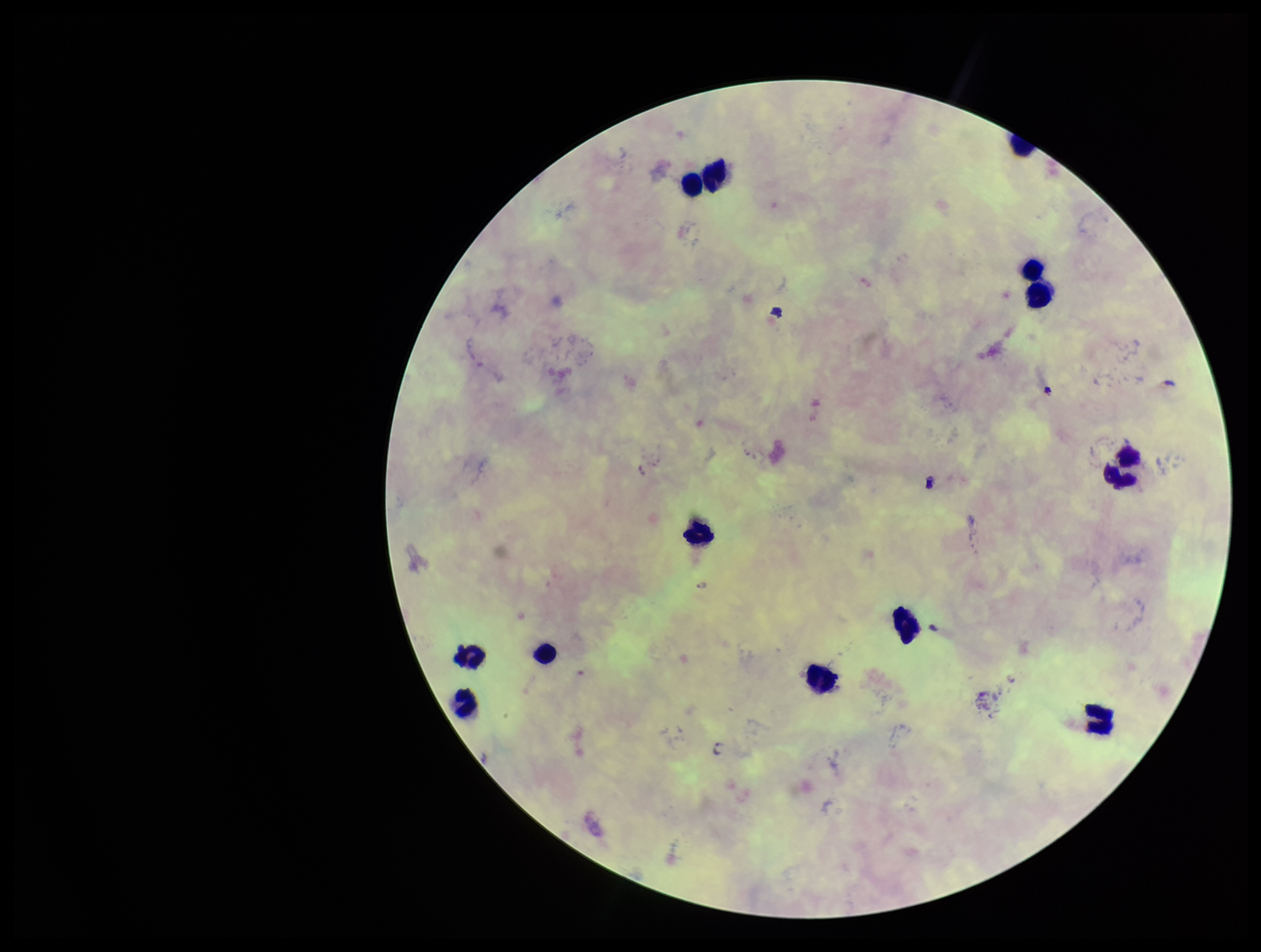
species_reported_for_this_patient: Plasmodium falciparum
field_of_view: one from this slide
leukocyte_count: 13
stain: Giemsa
image_size: 1261×952 pixels
capture: smartphone photograph through the microscope eyepiece
parasite_count: 0
patient_malaria_status: infected
preparation: thick
plasmodium_parasites: none identified